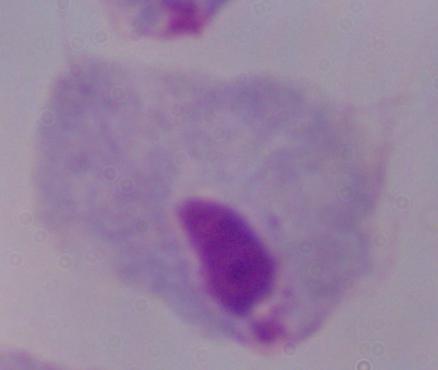

Summary:
  - Modality: photomicrograph
  - Identification: trichomonad
  - Magnification: 1000x